Report the malaria status of this cell.
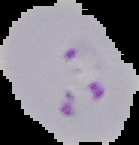
Parasitized.

From a thin blood smear. Segmented cell region on a black background. Image is 139×145 pixels.